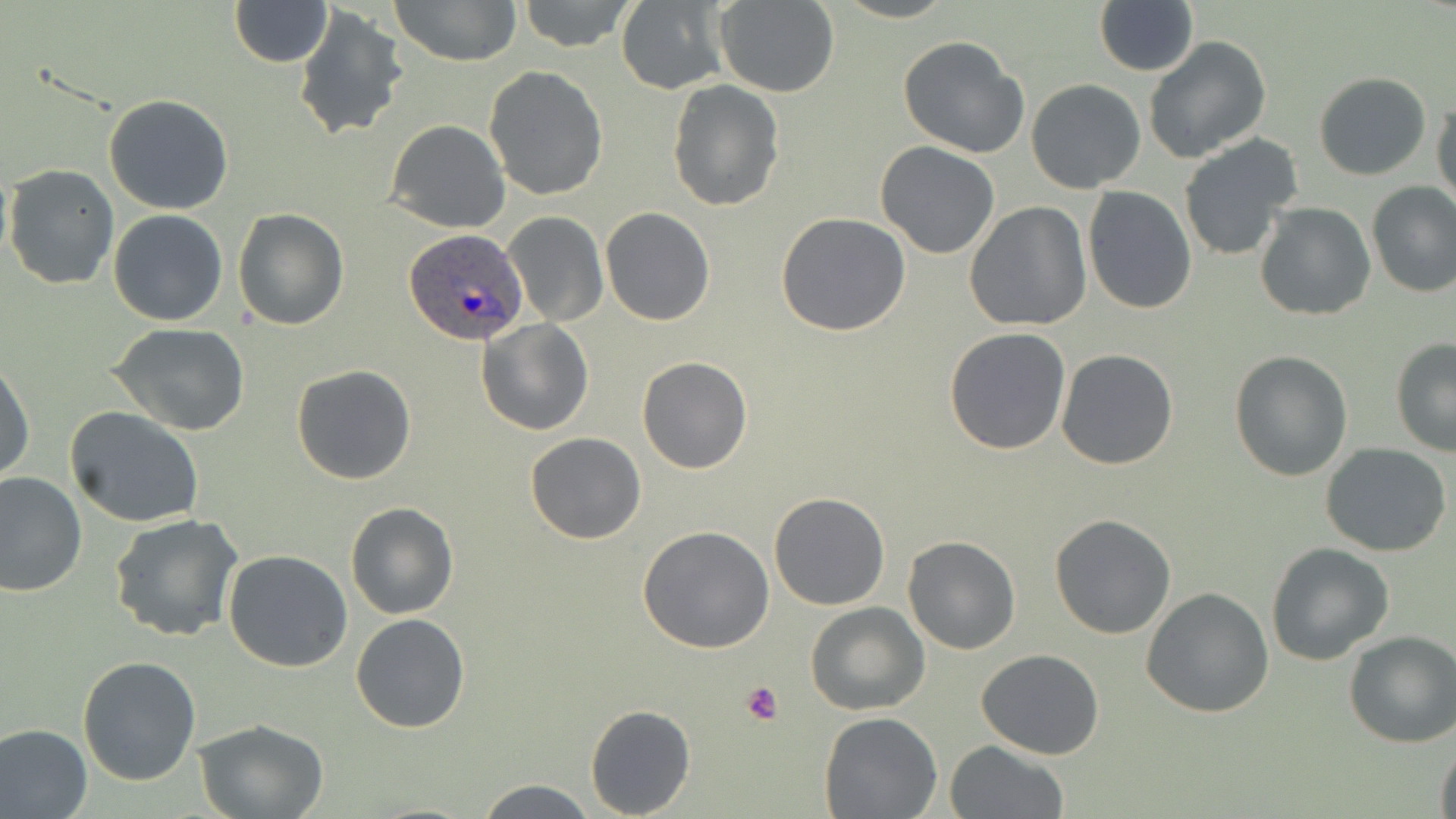

Summary:
  - Coordinate format: approximate bounding boxes as (x1, y1, x2, y2) in pixels
  - Uninfected red blood cell locations: (391, 0, 520, 67), (519, 0, 636, 52), (1094, 0, 1199, 76), (230, 1, 332, 67), (615, 1, 731, 92), (715, 1, 838, 97), (293, 5, 409, 142), (898, 36, 1029, 159), (1143, 36, 1272, 163), (484, 66, 608, 200), (1313, 71, 1431, 179), (665, 79, 784, 212), (1025, 79, 1146, 194), (103, 94, 234, 215), (1432, 95, 1455, 212), (385, 120, 509, 233), (1177, 134, 1302, 263), (875, 142, 1001, 259), (4, 164, 119, 290), (1366, 181, 1456, 298), (1082, 187, 1196, 315), (963, 203, 1093, 333), (1255, 203, 1376, 320), (601, 207, 715, 326), (233, 208, 348, 330), (109, 210, 227, 326), (503, 212, 607, 326), (776, 213, 912, 336), (477, 319, 593, 435), (109, 323, 252, 436), (944, 328, 1071, 455), (1390, 340, 1456, 457), (1056, 348, 1179, 469), (1229, 350, 1352, 481), (637, 355, 753, 474), (0, 357, 35, 485), (291, 363, 417, 484), (64, 407, 205, 530), (525, 431, 646, 544), (1321, 443, 1452, 557), (0, 469, 88, 597), (769, 491, 890, 610), (346, 501, 459, 620), (110, 515, 244, 642), (1049, 515, 1176, 639), (637, 525, 775, 652), (903, 536, 1020, 655), (1266, 543, 1395, 664), (223, 549, 352, 673), (1141, 587, 1275, 718), (805, 603, 928, 715), (350, 613, 471, 733), (1343, 632, 1456, 748), (977, 647, 1104, 760), (77, 656, 202, 786), (585, 704, 695, 817), (820, 710, 943, 818), (195, 718, 331, 818), (0, 724, 93, 819), (1435, 737, 1456, 819), (945, 741, 1068, 819), (473, 777, 597, 817)
  - Platelet locations: (739, 679, 784, 726)
  - Plasmodium ovale-infected red blood cell locations: (406, 228, 527, 348)
  - Slide-level diagnosis: Plasmodium ovale
  - Modality: light microscopy
  - Magnification: 1000x
  - Preparation: thin blood smear
  - Field of view: one of a larger specimen
  - Stain: May-Grünwald-Giemsa
  - Image size: 1456×819 pixels